Classify this cell by malaria status.
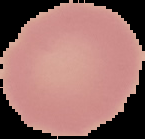
Uninfected.

Summary:
  - Preparation: thin blood smear
  - Image type: segmented cell region on a black background
  - Image size: 145×139 pixels